Report the malaria status of this cell.
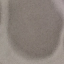

It is uninfected.

Photographed with a smartphone camera at the microscope eyepiece. Giemsa stain. Automatically extracted cell patch, resized to 64 × 64 pixels. Thin smear of blood.